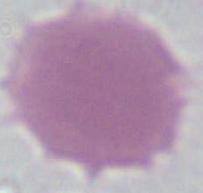
Summary:
  - Modality: micrograph
  - Identification: red blood cell
  - Magnification: 1000x